Describe the morphology of the red blood cells.
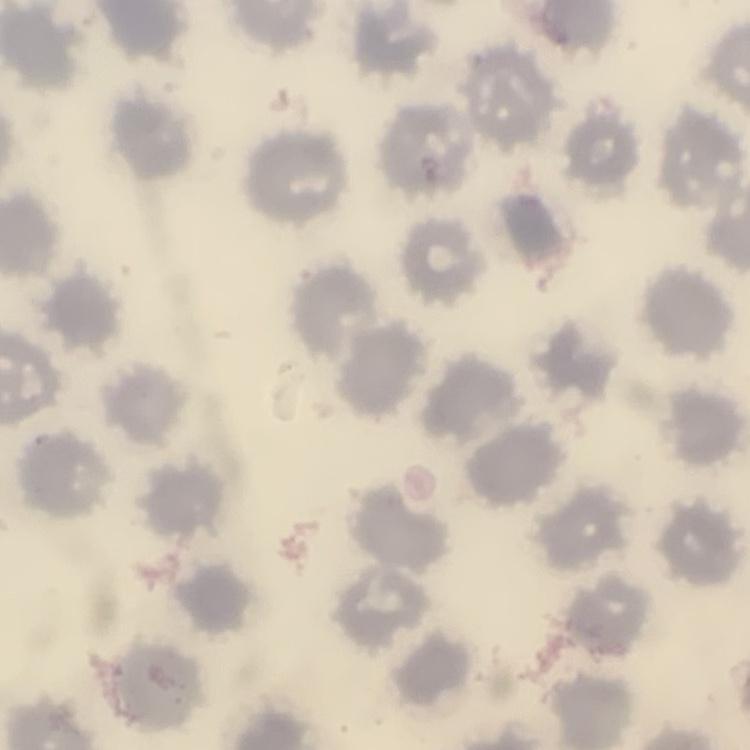
They show no rouleaux formation.

One tile cut from a larger photomicrograph. Thin peripheral smear. Field's or Giemsa stain.